Locate every Babesia divergens-infected red blood cell.
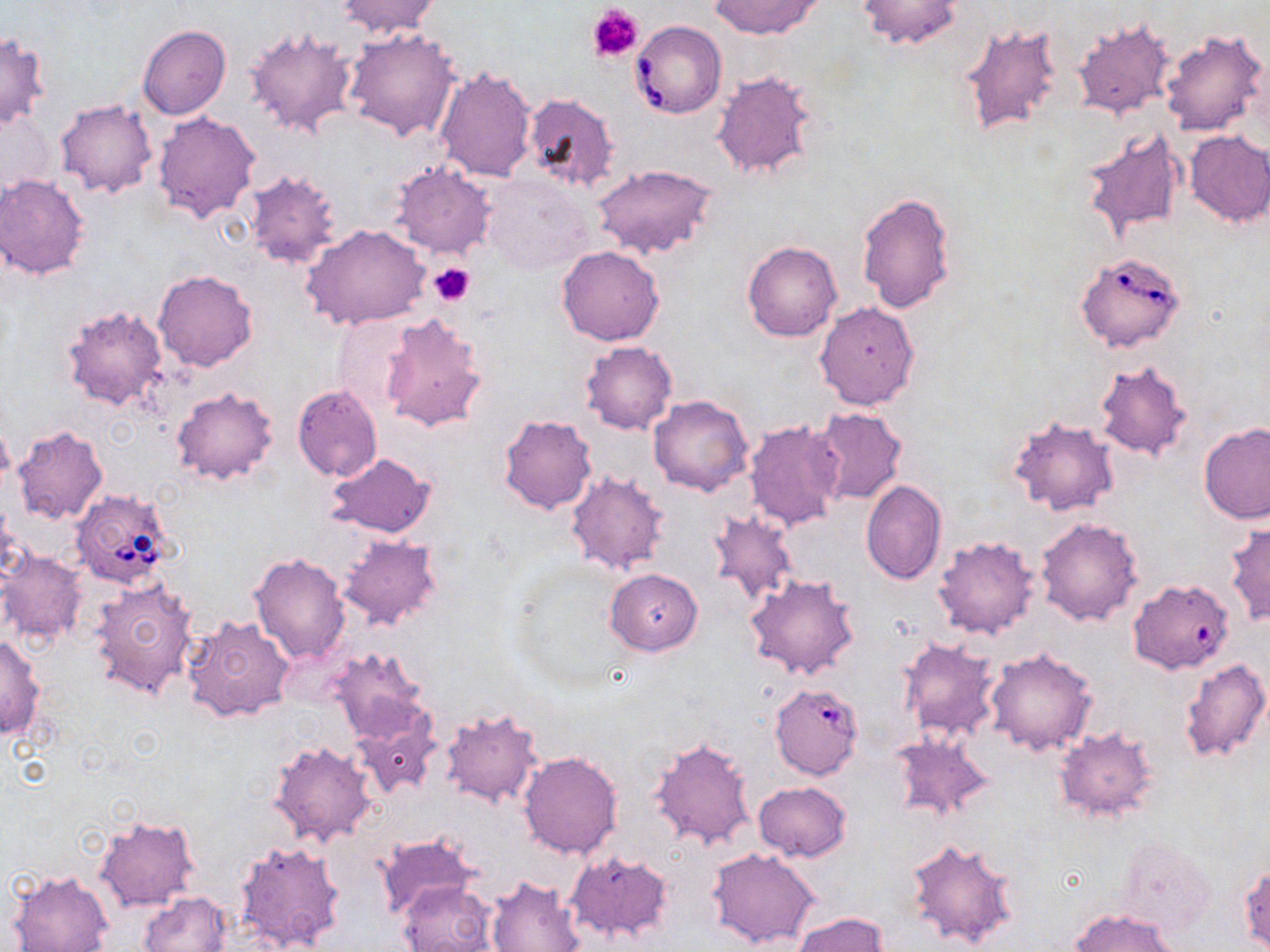
Approximate bounding boxes as (x1,y1)-(x2,y2) corner pairs in pixels.
Babesia divergens-infected red blood cells: (630,21)-(726,118), (1076,250)-(1187,353), (70,488)-(177,589), (1128,579)-(1234,674), (769,682)-(863,779).

Summary:
  - Platelet locations: (587,5)-(643,62), (428,260)-(474,307)
  - Uninfected red blood cell locations: (335,0)-(441,39), (710,0)-(823,38), (856,0)-(963,50), (1070,17)-(1177,123), (959,21)-(1066,139), (138,24)-(231,121), (244,26)-(359,140), (342,28)-(463,142), (1159,28)-(1269,139), (0,33)-(49,130), (434,67)-(536,179), (710,68)-(818,183), (521,91)-(620,193), (55,99)-(157,199), (152,110)-(261,224), (1,112)-(54,193), (1080,124)-(1189,242), (1182,130)-(1270,227), (389,162)-(497,259), (591,163)-(718,260), (244,170)-(345,269), (481,172)-(594,274), (0,174)-(90,279), (250,187)-(372,313), (856,192)-(957,314), (303,226)-(430,330), (742,240)-(842,342), (556,246)-(665,346), (154,270)-(258,371), (814,301)-(920,411), (59,302)-(171,413), (378,314)-(488,431), (331,316)-(416,416), (581,340)-(677,435), (1093,361)-(1195,463), (292,384)-(381,481), (172,387)-(278,486), (649,396)-(752,497), (813,407)-(907,505), (499,414)-(597,514), (1008,417)-(1118,517), (744,420)-(843,533), (1198,423)-(1270,524), (11,427)-(107,525), (326,453)-(433,537), (566,470)-(670,577), (861,480)-(946,584), (706,507)-(798,610), (1034,516)-(1143,626), (1225,521)-(1270,627), (335,534)-(442,633), (932,535)-(1040,640), (1,551)-(88,648), (247,551)-(350,665), (606,568)-(702,655), (744,573)-(860,681), (89,576)-(198,699), (181,614)-(296,722), (0,634)-(44,741), (895,638)-(1000,744), (325,647)-(431,745), (984,647)-(1098,757), (1179,657)-(1269,765), (438,710)-(545,808), (352,716)-(439,799), (1053,725)-(1160,822), (890,733)-(995,821), (650,736)-(757,851), (268,739)-(380,846), (518,751)-(622,859), (753,781)-(852,860), (93,815)-(200,913), (374,833)-(477,922), (1115,836)-(1217,937), (905,837)-(1019,950), (234,840)-(348,952), (707,847)-(820,950), (566,848)-(673,942), (1239,862)-(1269,950), (7,871)-(112,952), (484,876)-(584,952), (398,881)-(496,952), (138,891)-(233,952), (1070,908)-(1176,952), (791,910)-(889,951)
  - Slide-level diagnosis: Babesia divergens
  - Stain: May-Grünwald-Giemsa
  - Image size: 1270×952 pixels
  - Preparation: thin blood smear
  - Field of view: one of a larger specimen
  - Modality: light microscopy
  - Magnification: 1000x